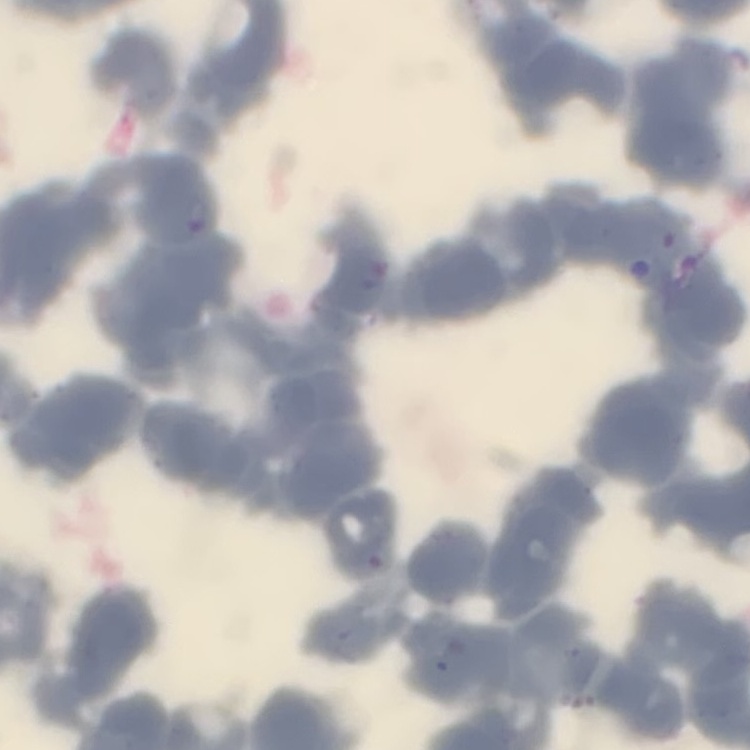
{
  "erythrocyte_morphology": "rouleaux formation",
  "image_type": "one tile cut from a larger photomicrograph",
  "stain": "Field's or Giemsa",
  "preparation": "thin blood smear"
}